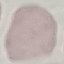
Summary:
  - Result: no malaria parasites detected
  - Capture: smartphone camera at the microscope eyepiece
  - Preparation: thin blood smear
  - Image type: automatically extracted cell patch, resized to 64 × 64 pixels
  - Stain: Giemsa